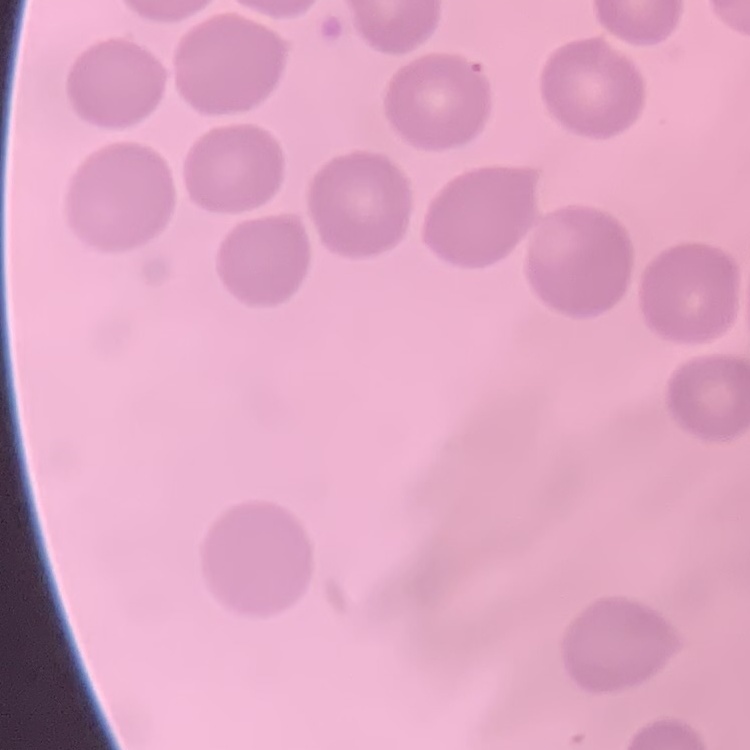
The erythrocytes exhibit no rouleaux formation. Thin peripheral smear. Field's or Giemsa stain. Square crop of a larger photomicrograph.